State the preparation type.
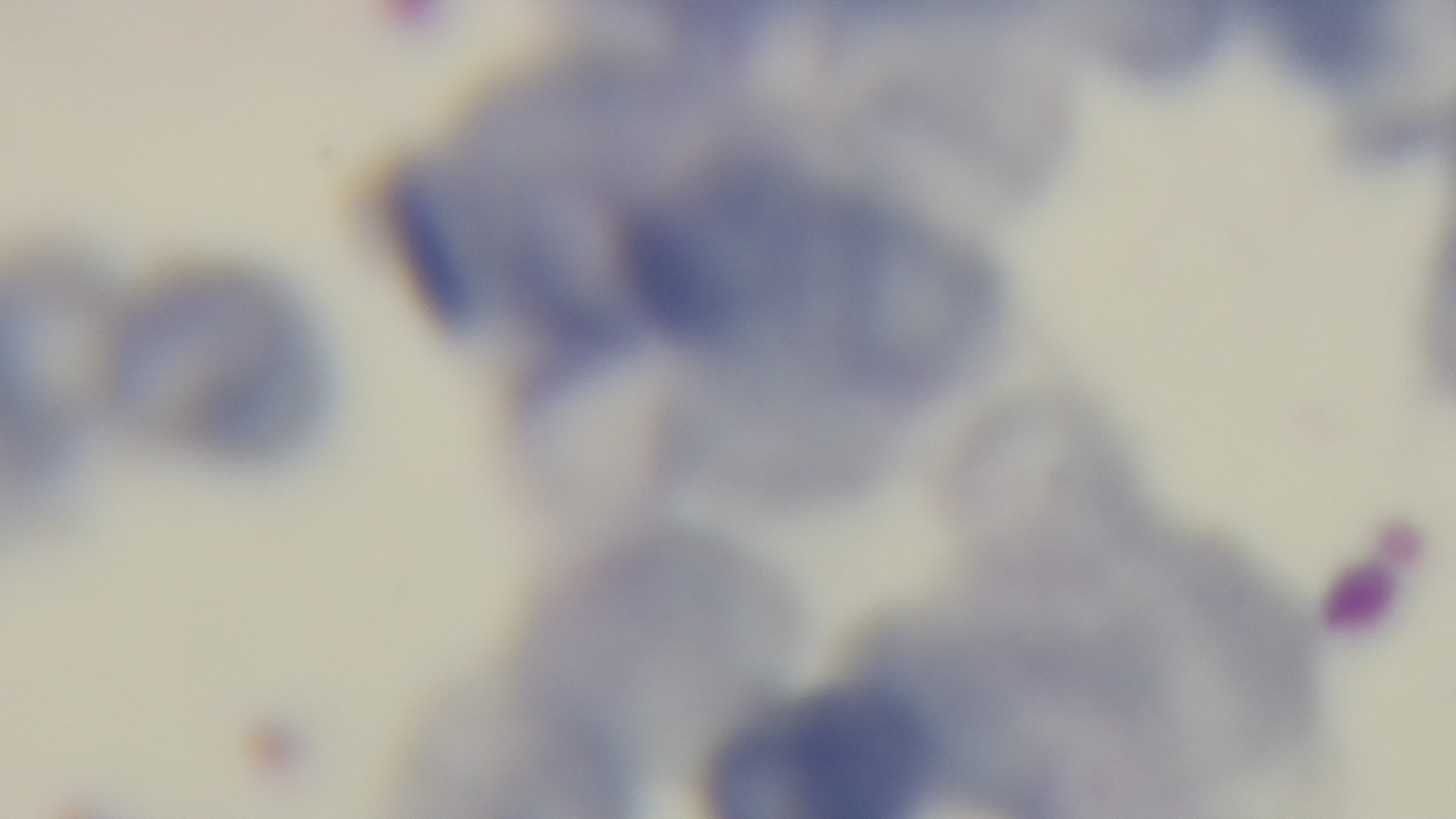
Thin.

Light microscopy. Malaria status: uninfected. Single field of view. Giemsa stain. 100x oil-immersion objective. Captured with a mounted 4K digital camera.